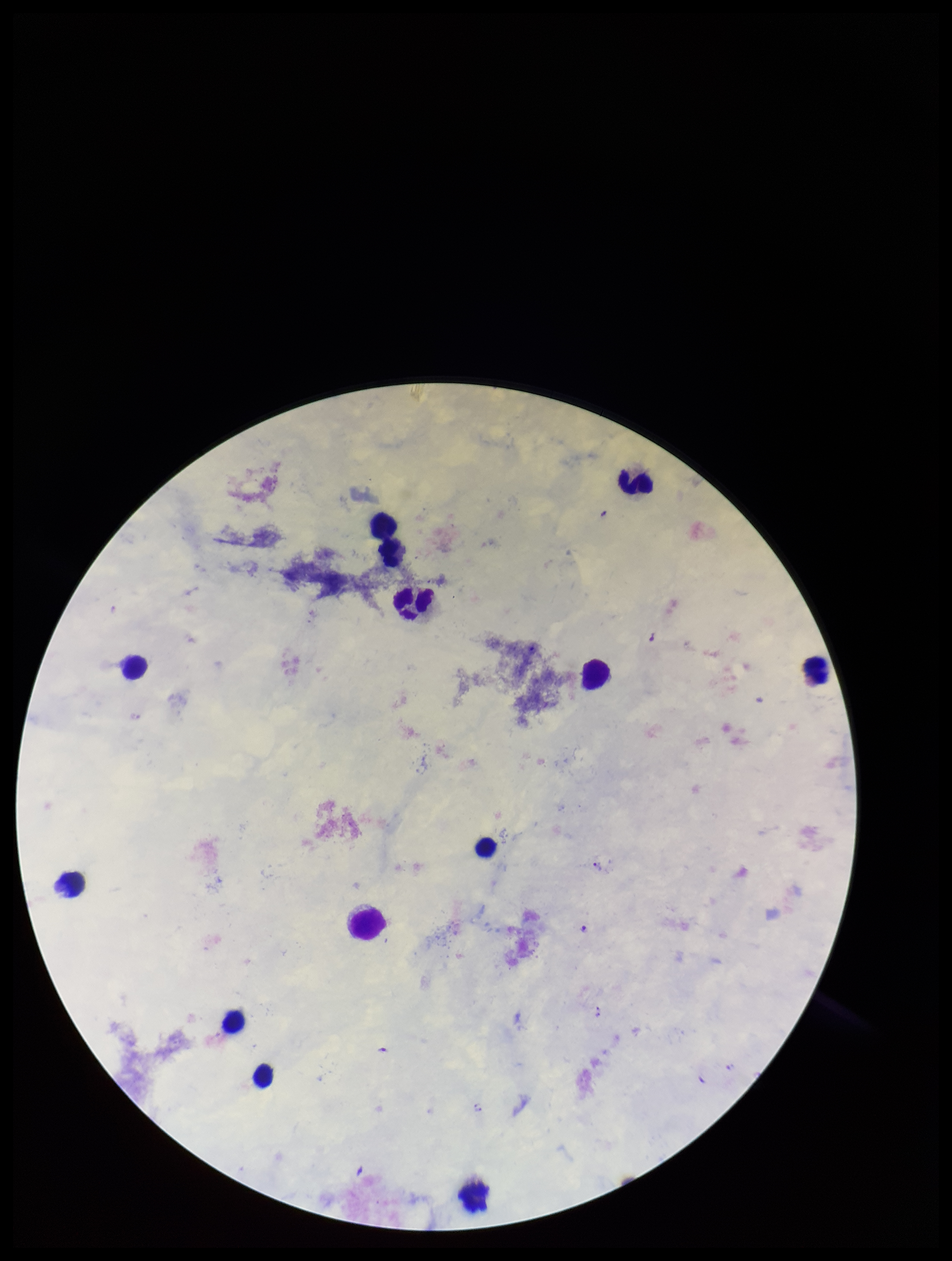

patient malaria status = positive
stain = Giemsa
species reported for this patient = Plasmodium falciparum
parasite count = 2
Plasmodium parasites = detected
image size = 952×1261 pixels
field of view = single
preparation = thick blood smear
leukocyte count = 13
capture = smartphone photograph through the microscope eyepiece